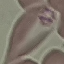

Summary:
  - Result: malaria parasites identified
  - Preparation: thin blood film
  - Image type: cell patch, automatically extracted from a larger field of view and resized to 64 × 64 pixels
  - Capture: smartphone camera at the microscope eyepiece
  - Stain: Giemsa